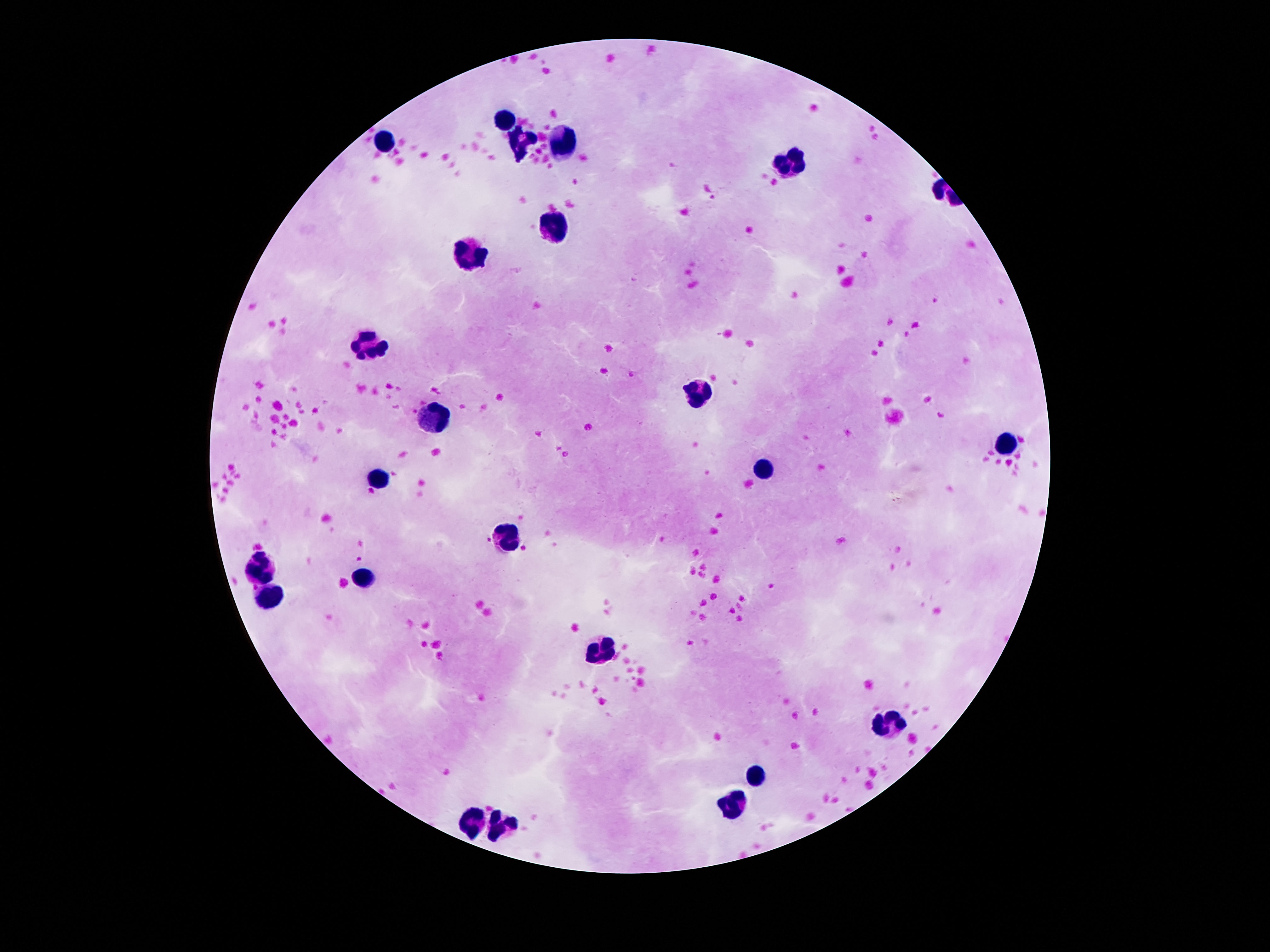

field_of_view: one from this slide
image_size: 1270×952 pixels
patient_malaria_status: not infected
stain: Giemsa
leukocyte_locations: 'approximate centers as [x, y] in pixels: [506, 119], [385, 141], [523, 143], [565, 145], [796, 163], [553, 227], [471, 254], [369, 344], [693, 393], [430, 416], [1005, 442], [763, 469], [380, 479], [508, 539], [261, 567], [359, 580], [270, 600], [600, 652], [889, 722], [754, 777], [733, 805], [476, 822], [504, 828]'
magnification: 100x
capture: smartphone camera through the microscope eyepiece
preparation: thick peripheral-blood smear